Comment on the morphology of the erythrocytes.
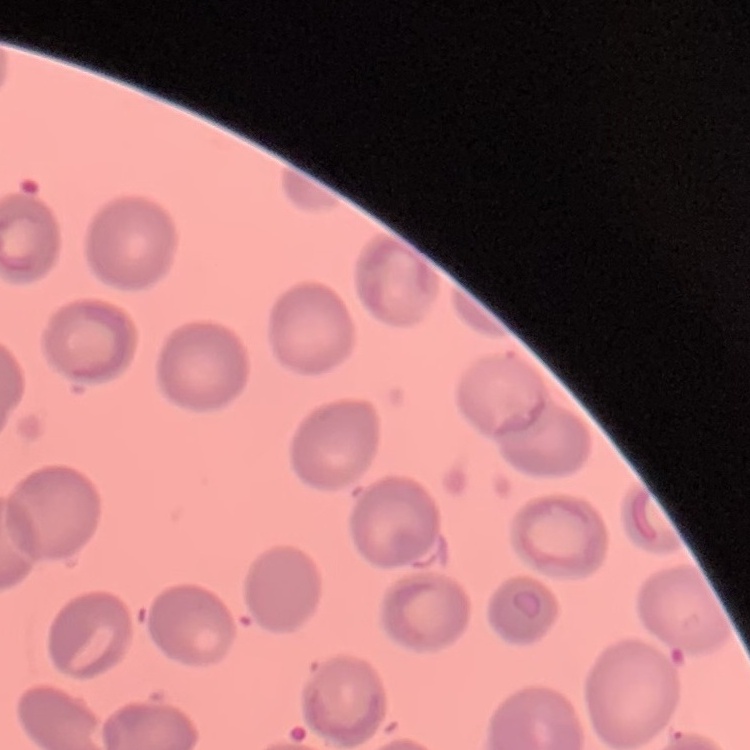

No rouleaux formation.

{
  "image_type": "one tile cut from a larger photomicrograph",
  "preparation": "thin peripheral smear",
  "stain": "Field's or Giemsa"
}